Report the malaria status of this cell.
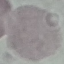

It is uninfected.

Acquired by smartphone through the microscope eyepiece. Cell patch, automatically extracted from a larger field of view and resized to 64 × 64 pixels. Giemsa stain. Thin blood smear.